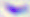
Summary:
  - Identification: Toxoplasma gondii
  - Magnification: 400x
  - Modality: micrograph